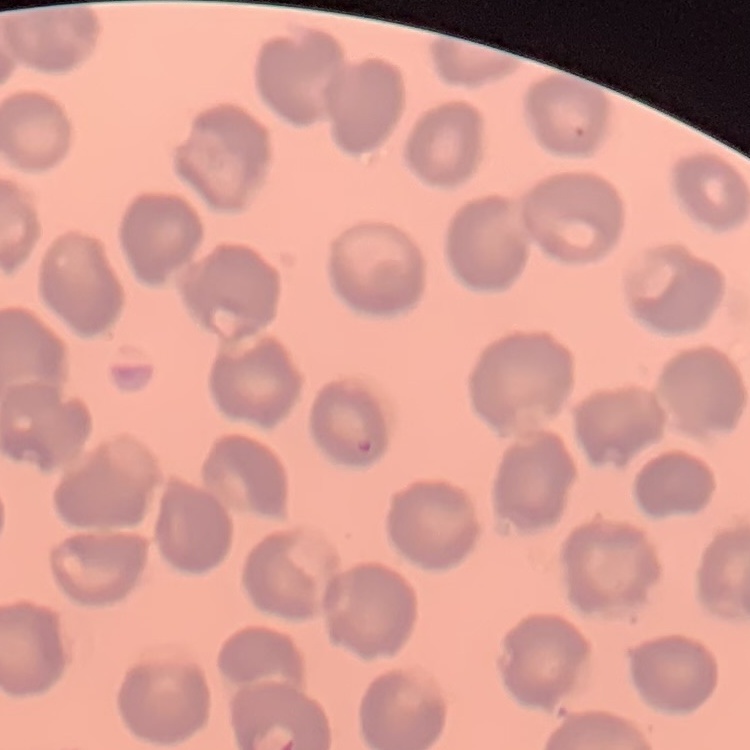 The erythrocytes show no rouleaux formation. Thin peripheral smear. One tile cut from a larger photomicrograph. Field's or Giemsa stain.